Outline each Plasmodium falciparum-infected red blood cell.
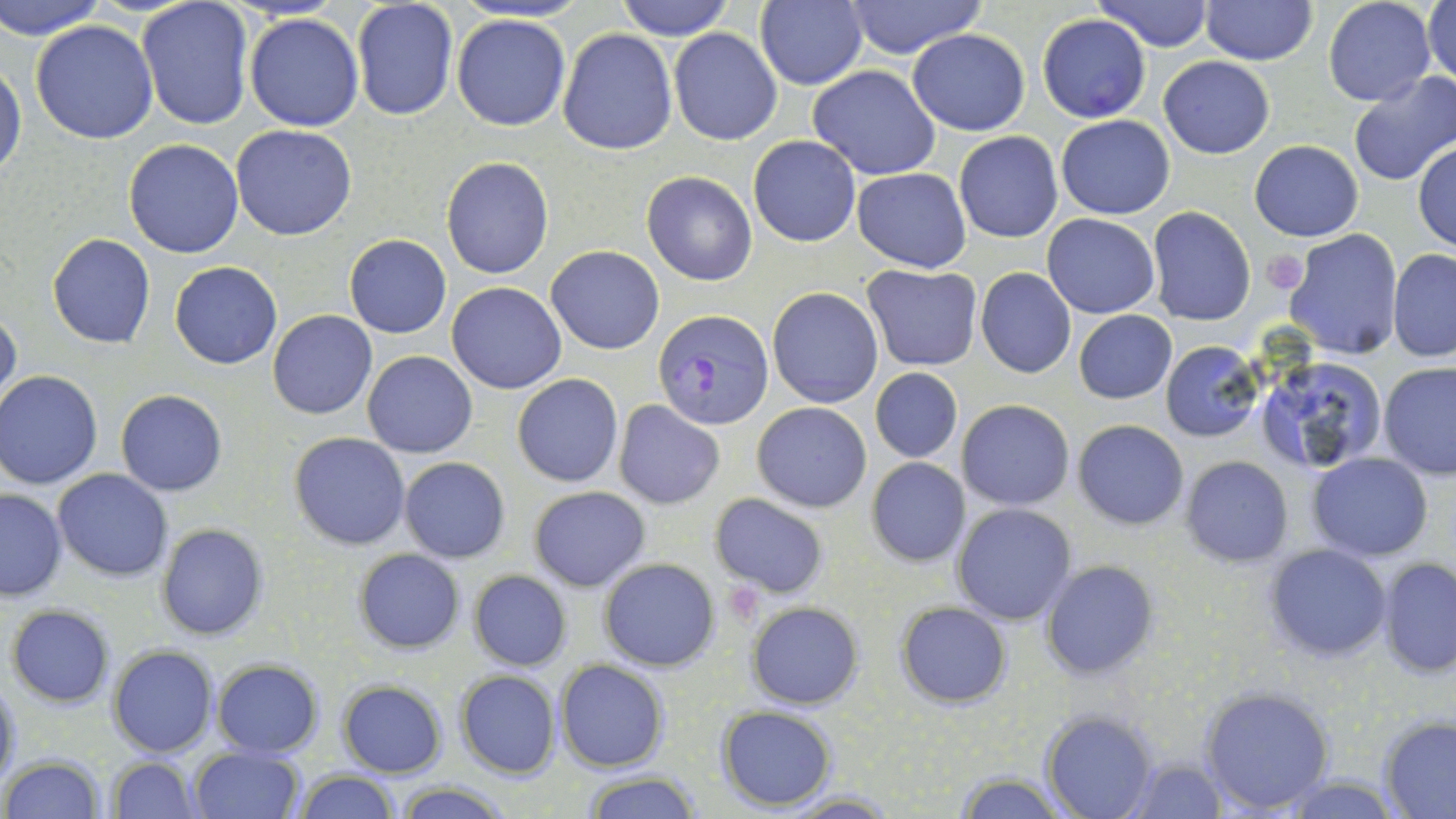

Approximate bounding boxes as [x1, y1, x2, y2] in pixels.
Plasmodium falciparum-infected red blood cells: [652, 309, 774, 431].

Platelet locations: [1261, 249, 1310, 293]. Uninfected red blood cell locations: [0, 0, 110, 40], [351, 0, 459, 122], [616, 0, 736, 41], [755, 0, 868, 90], [841, 0, 990, 58], [1095, 0, 1217, 52], [1201, 0, 1315, 65], [1323, 0, 1437, 106], [1425, 0, 1456, 86], [135, 3, 255, 133], [245, 13, 363, 131], [452, 14, 572, 131], [1037, 14, 1151, 122], [30, 20, 158, 143], [557, 28, 676, 155], [669, 28, 783, 146], [907, 30, 1030, 135], [1158, 55, 1275, 159], [0, 59, 27, 181], [809, 65, 941, 180], [1346, 71, 1456, 186], [1056, 115, 1174, 219], [230, 124, 359, 241], [953, 131, 1063, 243], [748, 135, 861, 247], [122, 138, 245, 258], [1249, 140, 1364, 240], [1413, 141, 1456, 252], [440, 156, 554, 280], [853, 167, 971, 272], [641, 171, 759, 287], [1148, 206, 1255, 325], [1042, 213, 1161, 319], [1282, 229, 1403, 359], [47, 233, 155, 349], [344, 234, 452, 338], [546, 245, 664, 355], [1387, 249, 1456, 362], [169, 262, 283, 369], [862, 265, 981, 370], [975, 268, 1076, 378], [447, 282, 567, 394], [767, 286, 885, 409], [0, 306, 22, 411], [268, 310, 376, 420], [1074, 310, 1176, 403], [1161, 341, 1263, 443], [361, 350, 478, 458], [1253, 353, 1392, 477], [1378, 362, 1456, 479], [870, 367, 962, 464], [0, 371, 103, 490], [512, 373, 623, 488], [116, 390, 226, 496], [612, 399, 725, 509], [956, 399, 1076, 511], [751, 401, 871, 513], [1073, 420, 1188, 530], [288, 432, 412, 550], [1308, 452, 1433, 561], [399, 457, 511, 563], [866, 457, 971, 567], [1181, 457, 1292, 567], [53, 469, 173, 581], [529, 485, 650, 591], [0, 487, 66, 602], [709, 494, 829, 598], [951, 502, 1077, 625], [155, 523, 267, 641], [1265, 544, 1391, 663], [352, 547, 465, 655], [1377, 557, 1455, 676], [599, 558, 719, 671], [1041, 560, 1159, 679], [468, 570, 572, 671], [895, 601, 1012, 708], [746, 602, 863, 710], [6, 605, 115, 708], [108, 645, 217, 756], [211, 659, 324, 757], [555, 660, 670, 771], [456, 670, 561, 779], [0, 676, 21, 793], [337, 680, 448, 778], [1200, 685, 1335, 815], [716, 706, 839, 810], [1041, 712, 1158, 819], [1378, 716, 1456, 818], [187, 746, 304, 819], [3, 756, 107, 819], [107, 756, 199, 818], [1122, 758, 1225, 817], [951, 771, 1067, 818], [294, 773, 400, 819], [583, 773, 701, 818], [1276, 775, 1402, 817], [391, 781, 516, 818], [786, 792, 902, 818]. Slide-level diagnosis: Plasmodium falciparum. One field of a larger specimen. Image is 1456×819 pixels. May-Grünwald-Giemsa stain. Captured at 1000x magnification. Thin blood smear. Optical microscopy.